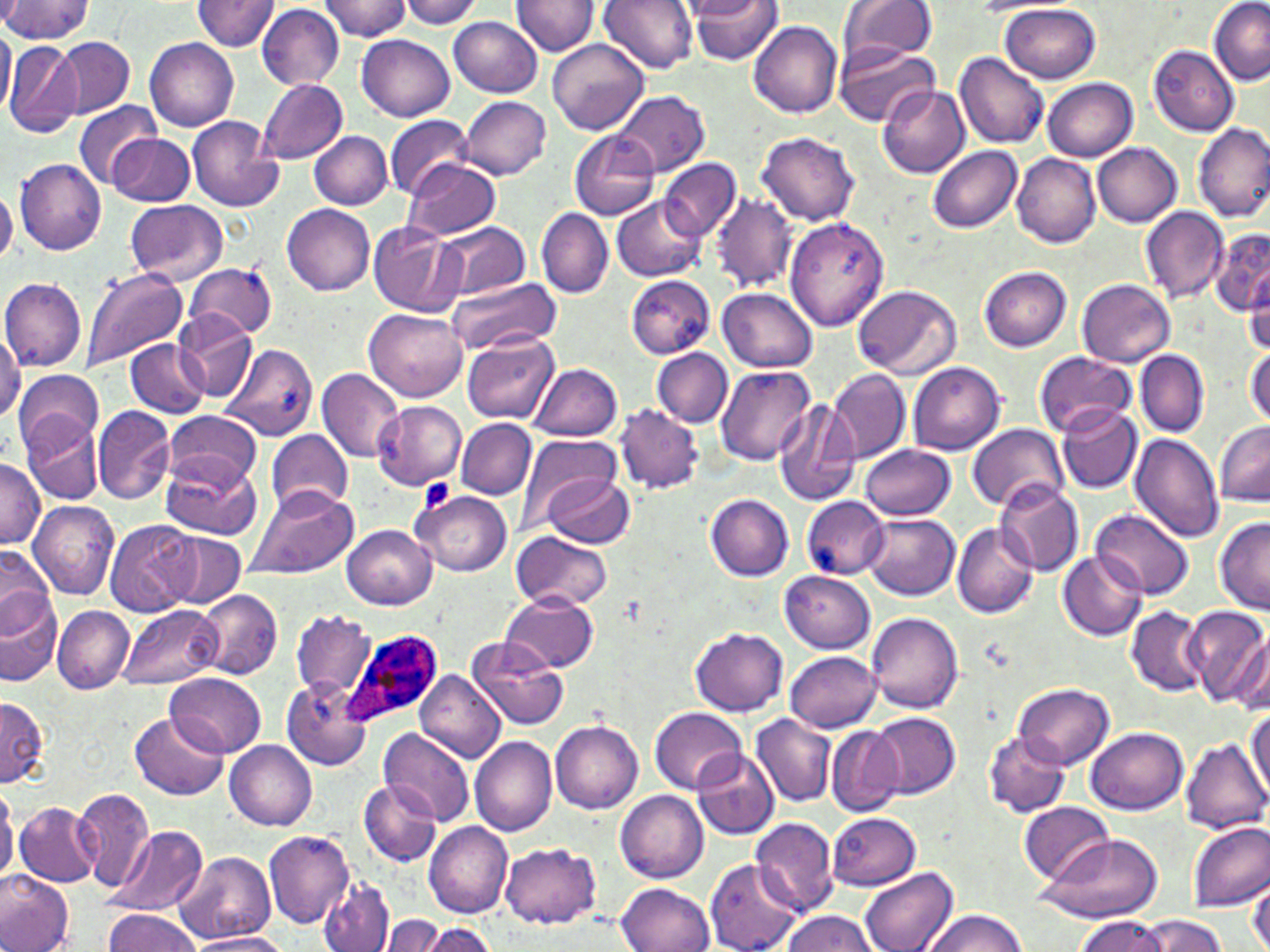

slide_level_diagnosis: Plasmodium ovale
stain: May-Grünwald-Giemsa
preparation: thin blood smear
plasmodium_ovale_infected_red_blood_cell_locations: 'approximate bounding boxes as named x1/y1/x2/y2 corners in pixels: (x1=342, y1=628, x2=445, y2=728)'
uninfected_red_blood_cell_locations: 'approximate bounding boxes as named x1/y1/x2/y2 corners in pixels: (x1=193, y1=0, x2=280, y2=51), (x1=317, y1=0, x2=416, y2=40), (x1=400, y1=0, x2=484, y2=29), (x1=511, y1=0, x2=598, y2=56), (x1=597, y1=0, x2=698, y2=73), (x1=836, y1=0, x2=939, y2=66), (x1=1209, y1=0, x2=1270, y2=84), (x1=0, y1=1, x2=92, y2=42), (x1=690, y1=1, x2=784, y2=66), (x1=974, y1=1, x2=1070, y2=14), (x1=1001, y1=3, x2=1101, y2=83), (x1=256, y1=4, x2=344, y2=89), (x1=448, y1=17, x2=543, y2=98), (x1=749, y1=21, x2=843, y2=117), (x1=0, y1=23, x2=15, y2=120), (x1=357, y1=32, x2=455, y2=121), (x1=53, y1=37, x2=134, y2=118), (x1=145, y1=38, x2=240, y2=132), (x1=548, y1=39, x2=649, y2=135), (x1=3, y1=42, x2=82, y2=137), (x1=1148, y1=45, x2=1240, y2=136), (x1=834, y1=46, x2=938, y2=128), (x1=955, y1=53, x2=1052, y2=148), (x1=258, y1=79, x2=349, y2=163), (x1=1042, y1=79, x2=1137, y2=161), (x1=877, y1=84, x2=971, y2=179), (x1=614, y1=90, x2=709, y2=177), (x1=460, y1=96, x2=551, y2=179), (x1=73, y1=100, x2=162, y2=190), (x1=186, y1=114, x2=283, y2=212), (x1=385, y1=116, x2=473, y2=198), (x1=1194, y1=122, x2=1270, y2=221), (x1=570, y1=131, x2=661, y2=220), (x1=757, y1=131, x2=859, y2=227), (x1=309, y1=132, x2=393, y2=209), (x1=108, y1=133, x2=194, y2=206), (x1=1093, y1=144, x2=1182, y2=227), (x1=927, y1=145, x2=1023, y2=233), (x1=1013, y1=153, x2=1101, y2=247), (x1=660, y1=157, x2=742, y2=241), (x1=15, y1=158, x2=106, y2=255), (x1=403, y1=160, x2=502, y2=241), (x1=0, y1=186, x2=17, y2=264), (x1=711, y1=191, x2=799, y2=292), (x1=612, y1=196, x2=705, y2=282), (x1=124, y1=199, x2=228, y2=286), (x1=281, y1=204, x2=374, y2=295), (x1=1140, y1=206, x2=1229, y2=304), (x1=537, y1=208, x2=612, y2=297), (x1=784, y1=216, x2=890, y2=331), (x1=368, y1=221, x2=463, y2=317), (x1=434, y1=221, x2=529, y2=300), (x1=1211, y1=228, x2=1270, y2=318), (x1=185, y1=260, x2=278, y2=337), (x1=979, y1=266, x2=1072, y2=352), (x1=81, y1=268, x2=187, y2=373), (x1=1244, y1=269, x2=1270, y2=357), (x1=1, y1=276, x2=86, y2=372), (x1=626, y1=276, x2=717, y2=358), (x1=444, y1=277, x2=560, y2=358), (x1=1077, y1=278, x2=1176, y2=367), (x1=853, y1=284, x2=961, y2=379), (x1=719, y1=287, x2=819, y2=371), (x1=365, y1=307, x2=466, y2=402), (x1=172, y1=310, x2=257, y2=402), (x1=0, y1=332, x2=22, y2=420), (x1=462, y1=334, x2=560, y2=423), (x1=123, y1=338, x2=210, y2=418), (x1=220, y1=343, x2=317, y2=440), (x1=653, y1=347, x2=733, y2=428), (x1=1246, y1=347, x2=1270, y2=427), (x1=1134, y1=349, x2=1210, y2=437), (x1=1033, y1=351, x2=1136, y2=437), (x1=530, y1=363, x2=623, y2=442), (x1=908, y1=363, x2=1005, y2=456), (x1=717, y1=366, x2=817, y2=465), (x1=316, y1=368, x2=405, y2=463), (x1=13, y1=369, x2=103, y2=455), (x1=828, y1=369, x2=911, y2=466), (x1=772, y1=397, x2=862, y2=507), (x1=373, y1=401, x2=466, y2=490), (x1=92, y1=404, x2=177, y2=506), (x1=615, y1=404, x2=705, y2=494), (x1=1056, y1=405, x2=1142, y2=495), (x1=164, y1=409, x2=261, y2=490), (x1=23, y1=414, x2=104, y2=503), (x1=457, y1=418, x2=537, y2=498), (x1=1215, y1=422, x2=1270, y2=506), (x1=966, y1=424, x2=1068, y2=514), (x1=266, y1=429, x2=353, y2=514), (x1=515, y1=434, x2=620, y2=527), (x1=1131, y1=434, x2=1225, y2=541), (x1=862, y1=443, x2=957, y2=519), (x1=0, y1=457, x2=43, y2=546), (x1=161, y1=457, x2=260, y2=539), (x1=541, y1=473, x2=634, y2=548), (x1=994, y1=480, x2=1085, y2=576), (x1=246, y1=484, x2=357, y2=579), (x1=411, y1=491, x2=512, y2=577), (x1=706, y1=493, x2=796, y2=580), (x1=801, y1=496, x2=891, y2=579), (x1=28, y1=500, x2=119, y2=598), (x1=1093, y1=507, x2=1193, y2=600), (x1=862, y1=512, x2=960, y2=600), (x1=1215, y1=517, x2=1270, y2=612), (x1=105, y1=520, x2=197, y2=616), (x1=952, y1=523, x2=1040, y2=619), (x1=341, y1=524, x2=436, y2=609), (x1=511, y1=529, x2=614, y2=613), (x1=162, y1=530, x2=246, y2=607), (x1=0, y1=546, x2=55, y2=635), (x1=1059, y1=553, x2=1148, y2=640), (x1=779, y1=572, x2=876, y2=654), (x1=194, y1=591, x2=282, y2=680), (x1=501, y1=592, x2=598, y2=671), (x1=0, y1=593, x2=62, y2=688), (x1=120, y1=604, x2=220, y2=689), (x1=52, y1=605, x2=133, y2=694), (x1=1126, y1=605, x2=1210, y2=697), (x1=1184, y1=606, x2=1270, y2=708), (x1=289, y1=610, x2=376, y2=701), (x1=867, y1=610, x2=963, y2=713), (x1=1221, y1=626, x2=1270, y2=714), (x1=691, y1=629, x2=788, y2=715), (x1=468, y1=635, x2=569, y2=732), (x1=785, y1=650, x2=882, y2=733), (x1=416, y1=670, x2=506, y2=763), (x1=166, y1=672, x2=265, y2=758), (x1=281, y1=678, x2=374, y2=771), (x1=1013, y1=683, x2=1115, y2=768), (x1=1, y1=694, x2=50, y2=788), (x1=1247, y1=705, x2=1269, y2=799), (x1=648, y1=707, x2=747, y2=795), (x1=131, y1=712, x2=229, y2=800), (x1=869, y1=712, x2=960, y2=798), (x1=751, y1=715, x2=835, y2=805), (x1=550, y1=720, x2=643, y2=814), (x1=826, y1=726, x2=905, y2=817), (x1=1087, y1=727, x2=1188, y2=815), (x1=378, y1=728, x2=473, y2=826), (x1=983, y1=731, x2=1072, y2=819), (x1=470, y1=736, x2=557, y2=836), (x1=1180, y1=738, x2=1270, y2=835), (x1=225, y1=740, x2=318, y2=830), (x1=692, y1=749, x2=780, y2=840), (x1=358, y1=782, x2=441, y2=866), (x1=73, y1=787, x2=154, y2=891), (x1=617, y1=790, x2=709, y2=883), (x1=5, y1=799, x2=85, y2=947), (x1=15, y1=802, x2=103, y2=886), (x1=1019, y1=802, x2=1114, y2=883), (x1=828, y1=812, x2=921, y2=890), (x1=750, y1=817, x2=840, y2=915), (x1=423, y1=819, x2=513, y2=918), (x1=1187, y1=821, x2=1270, y2=913), (x1=111, y1=824, x2=210, y2=917), (x1=263, y1=830, x2=354, y2=927), (x1=1028, y1=831, x2=1164, y2=925), (x1=500, y1=843, x2=600, y2=926), (x1=175, y1=851, x2=275, y2=945), (x1=705, y1=860, x2=803, y2=952), (x1=859, y1=866, x2=959, y2=952), (x1=0, y1=871, x2=73, y2=952), (x1=1248, y1=875, x2=1270, y2=952), (x1=319, y1=876, x2=395, y2=952), (x1=616, y1=882, x2=714, y2=952), (x1=103, y1=909, x2=200, y2=951), (x1=921, y1=909, x2=1026, y2=952), (x1=778, y1=911, x2=878, y2=952), (x1=380, y1=914, x2=448, y2=952), (x1=1075, y1=914, x2=1170, y2=951), (x1=1137, y1=914, x2=1228, y2=952), (x1=426, y1=924, x2=498, y2=952), (x1=186, y1=932, x2=288, y2=952)'
image_size: 1270×952 pixels
magnification: 1000x
platelet_locations: 'approximate bounding boxes as named x1/y1/x2/y2 corners in pixels: (x1=419, y1=480, x2=454, y2=511)'
field_of_view: single
modality: optical microscopy